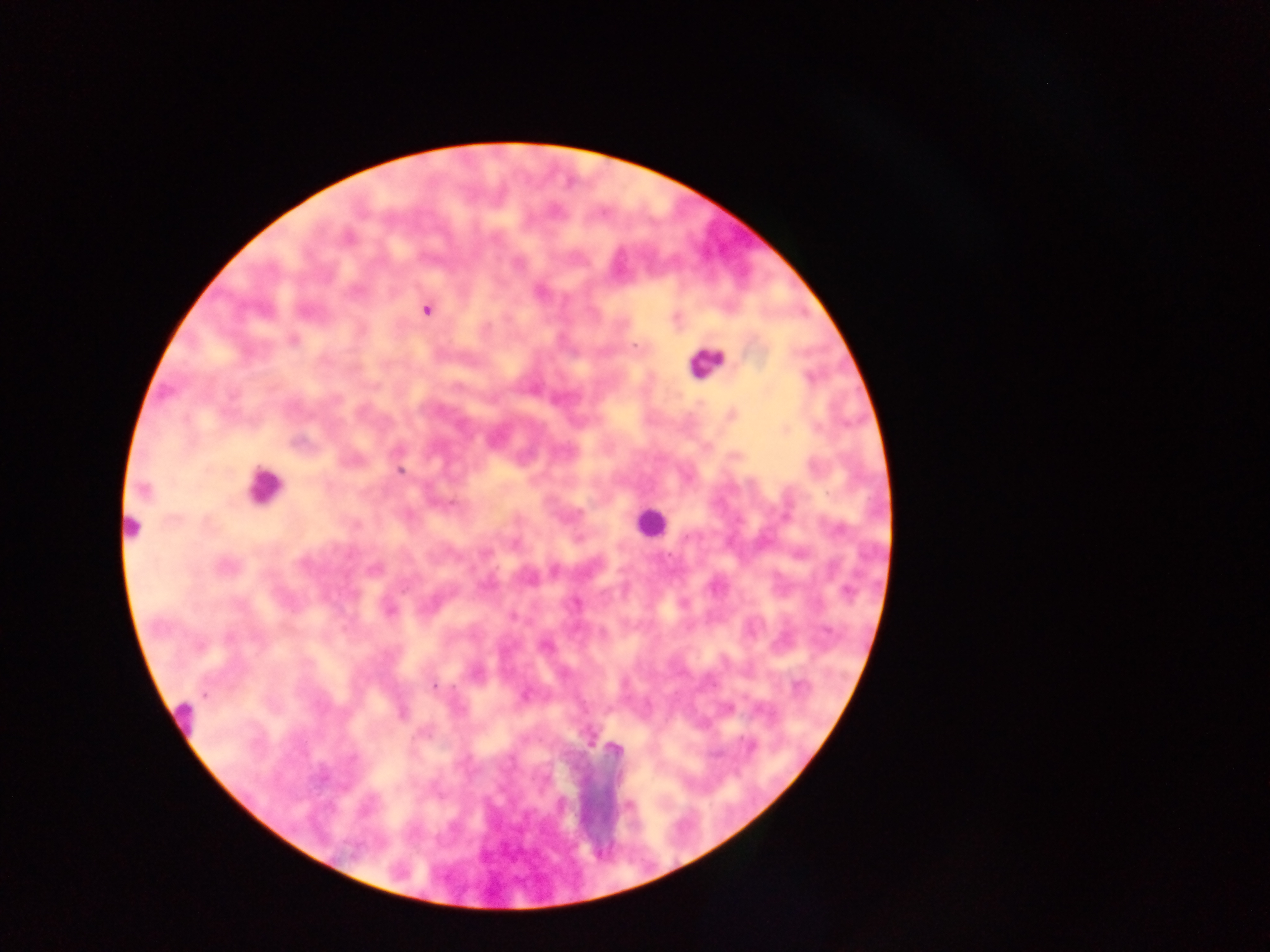

Approximate centers as x y in pixels.
Summary:
  - Leukocyte locations: 706 362; 264 486; 650 521; 131 526; 183 719; 591 796
  - Malaria parasite locations: 348 239; 426 310; 293 340; 634 346; 400 471; 143 490; 687 537; 226 566; 847 592; 390 612; 545 645; 434 686; 205 695; 749 745
  - Capture: mobile-phone photograph through a microscope
  - Preparation: thick blood film
  - Image size: 1270×952 pixels
  - Country: Ghana
  - Field of view: single